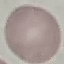
malaria status = uninfected
stain = Giemsa
image type = cell patch, automatically extracted from a larger field of view and resized to 64 × 64 pixels
preparation = thin blood film
capture = smartphone camera at the microscope eyepiece